Outline each Plasmodium vivax-infected red blood cell.
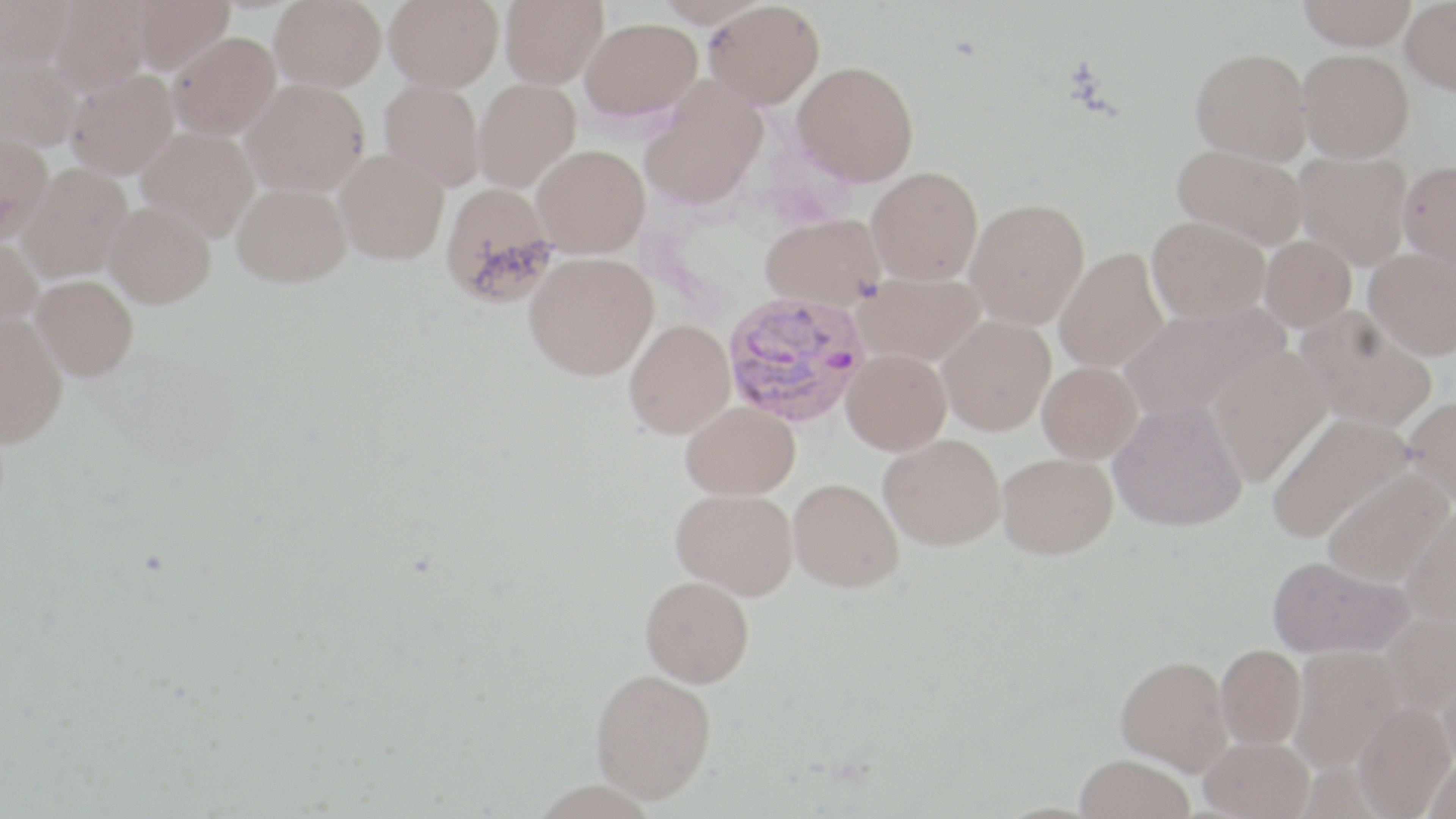

Approximate bounding boxes as [x1, y1, x2, y2] in pixels.
Plasmodium vivax-infected red blood cells: [721, 289, 870, 428].

Uninfected red blood cell locations: [1, 0, 77, 69], [51, 0, 152, 96], [130, 0, 236, 74], [269, 0, 386, 91], [383, 0, 504, 91], [500, 0, 608, 89], [654, 0, 767, 27], [1296, 0, 1416, 50], [1400, 0, 1456, 95], [704, 1, 825, 109], [581, 17, 702, 122], [167, 31, 280, 140], [1191, 47, 1312, 163], [1297, 49, 1414, 162], [0, 54, 82, 151], [793, 61, 919, 185], [67, 70, 179, 178], [473, 78, 580, 193], [242, 79, 369, 197], [379, 79, 486, 190], [639, 83, 767, 209], [137, 127, 260, 241], [0, 131, 52, 239], [1172, 142, 1307, 248], [532, 144, 650, 258], [335, 148, 450, 264], [1293, 150, 1413, 269], [1397, 160, 1456, 272], [18, 164, 132, 281], [867, 166, 983, 284], [231, 182, 351, 287], [440, 183, 559, 307], [965, 197, 1089, 328], [104, 202, 216, 308], [759, 213, 887, 311], [1147, 216, 1269, 322], [0, 235, 43, 330], [1259, 235, 1356, 331], [1055, 247, 1168, 373], [1364, 248, 1456, 360], [525, 251, 658, 380], [855, 270, 986, 366], [32, 275, 139, 380], [1120, 303, 1286, 421], [1295, 308, 1437, 432], [0, 314, 68, 447], [937, 314, 1055, 435], [624, 319, 735, 438], [1207, 345, 1332, 487], [842, 349, 951, 455], [1037, 361, 1142, 463], [1402, 395, 1456, 506], [1109, 399, 1247, 531], [681, 401, 799, 498], [1266, 411, 1413, 543], [879, 433, 1006, 550], [997, 451, 1117, 558], [1322, 469, 1451, 585], [788, 478, 903, 592], [671, 487, 798, 597], [1401, 507, 1456, 626], [1266, 555, 1413, 658], [640, 575, 754, 687], [1381, 613, 1456, 715], [1216, 644, 1306, 749], [1288, 646, 1405, 773], [1116, 656, 1232, 774], [590, 668, 716, 803], [1438, 668, 1456, 776], [1353, 702, 1455, 819], [1199, 736, 1314, 819], [1074, 754, 1196, 819], [1423, 758, 1456, 819]. Slide-level diagnosis: Plasmodium vivax. One field of a larger specimen. May-Grünwald-Giemsa-stained preparation. Thin blood smear. Image is 1456×819 pixels. Light microscopy. Captured at 1000x magnification.